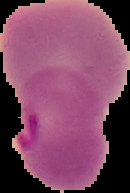

Summary:
  - Malaria status: parasitized
  - Image type: cell region segmented out of the field of view; surrounding area masked to black
  - Preparation: thin blood film
  - Image size: 130×193 pixels